Describe the morphology of the erythrocytes.
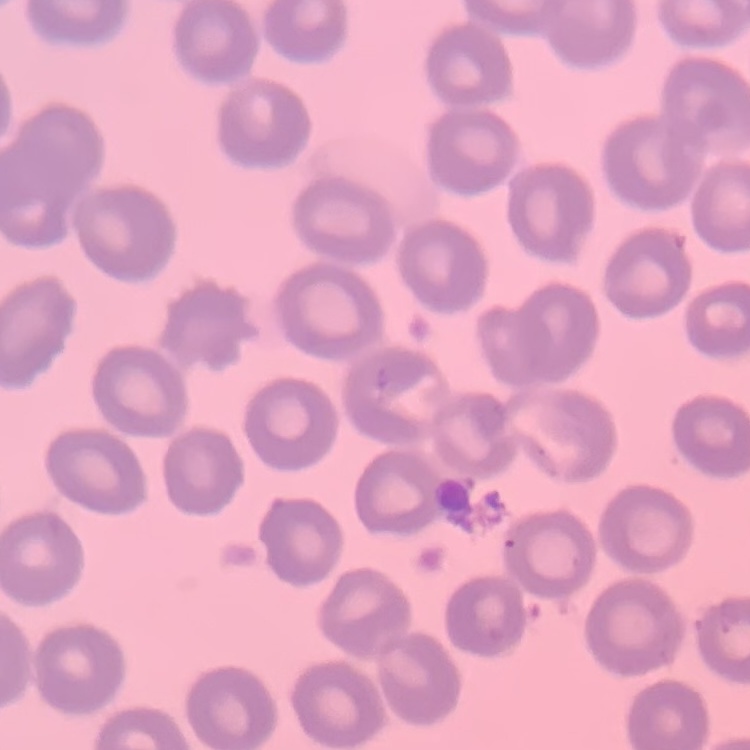
No rouleaux formation.

Square crop of a larger photomicrograph. Field's or Giemsa stain. Thin peripheral smear.